Point out each leukocyte.
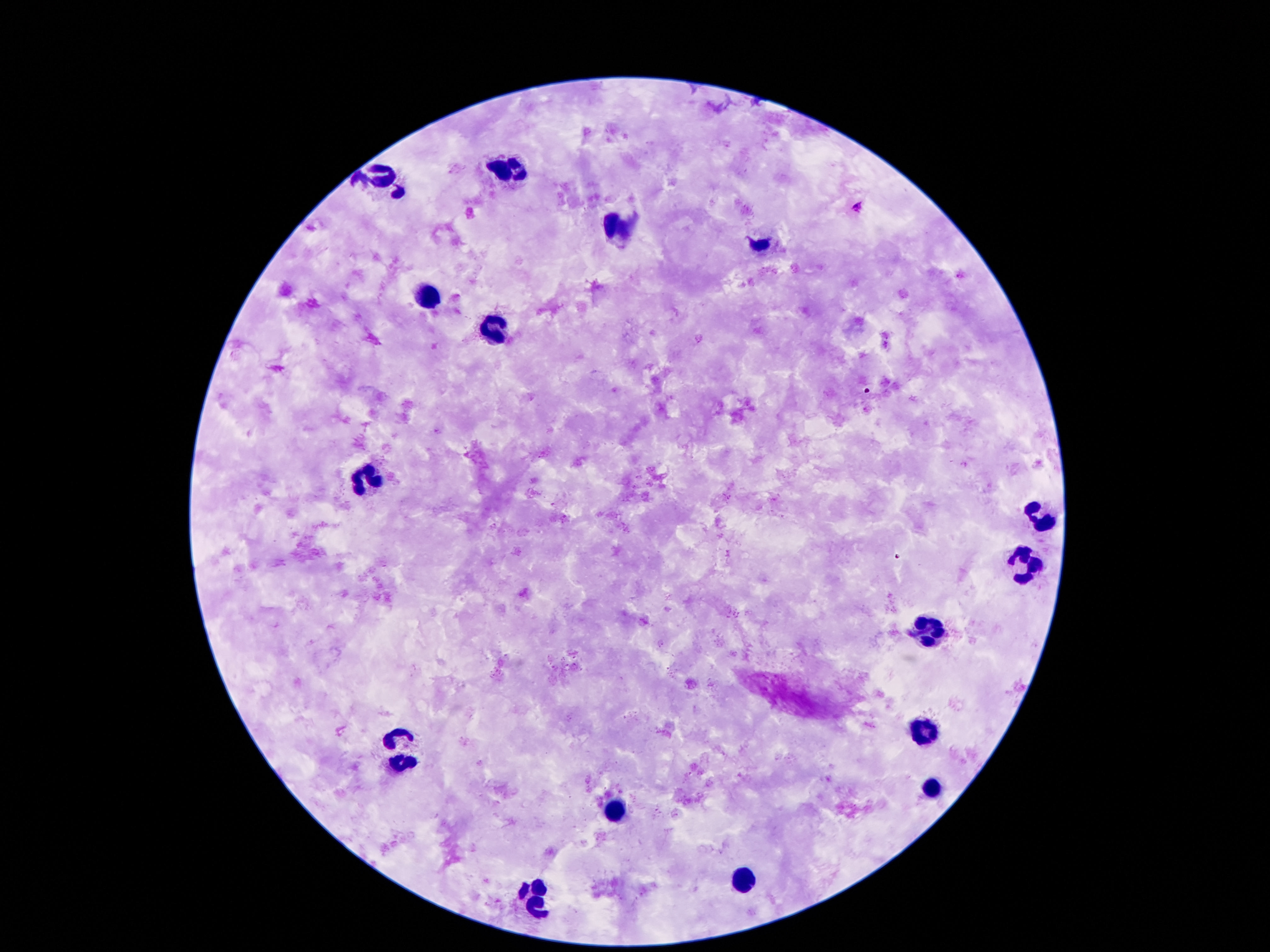
Approximate object centers, in pixels from the top-left corner.
Leukocytes: (x=508, y=170), (x=380, y=175), (x=618, y=229), (x=426, y=299), (x=496, y=327), (x=370, y=478), (x=1040, y=518), (x=1024, y=564), (x=931, y=634), (x=931, y=730), (x=403, y=747), (x=933, y=789), (x=616, y=814), (x=744, y=882), (x=536, y=900).

100x magnification. Photographed through the microscope eyepiece with a smartphone camera. Image is 1270×952 pixels. One field from this slide. Giemsa stain. Patient malaria status: not infected. Thick blood film.